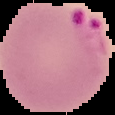

Summary:
  - Image type: cell region segmented out of the field of view; surrounding area masked to black
  - Preparation: thin blood film
  - Image size: 115×115 pixels
  - Result: malaria parasites detected